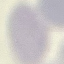

Summary:
  - Result: no malaria parasites seen
  - Image type: automatically extracted cell patch, resized to 64 × 64 pixels
  - Preparation: thin blood smear
  - Stain: Giemsa
  - Capture: smartphone through the microscope eyepiece